Point out each Plasmodium parasite.
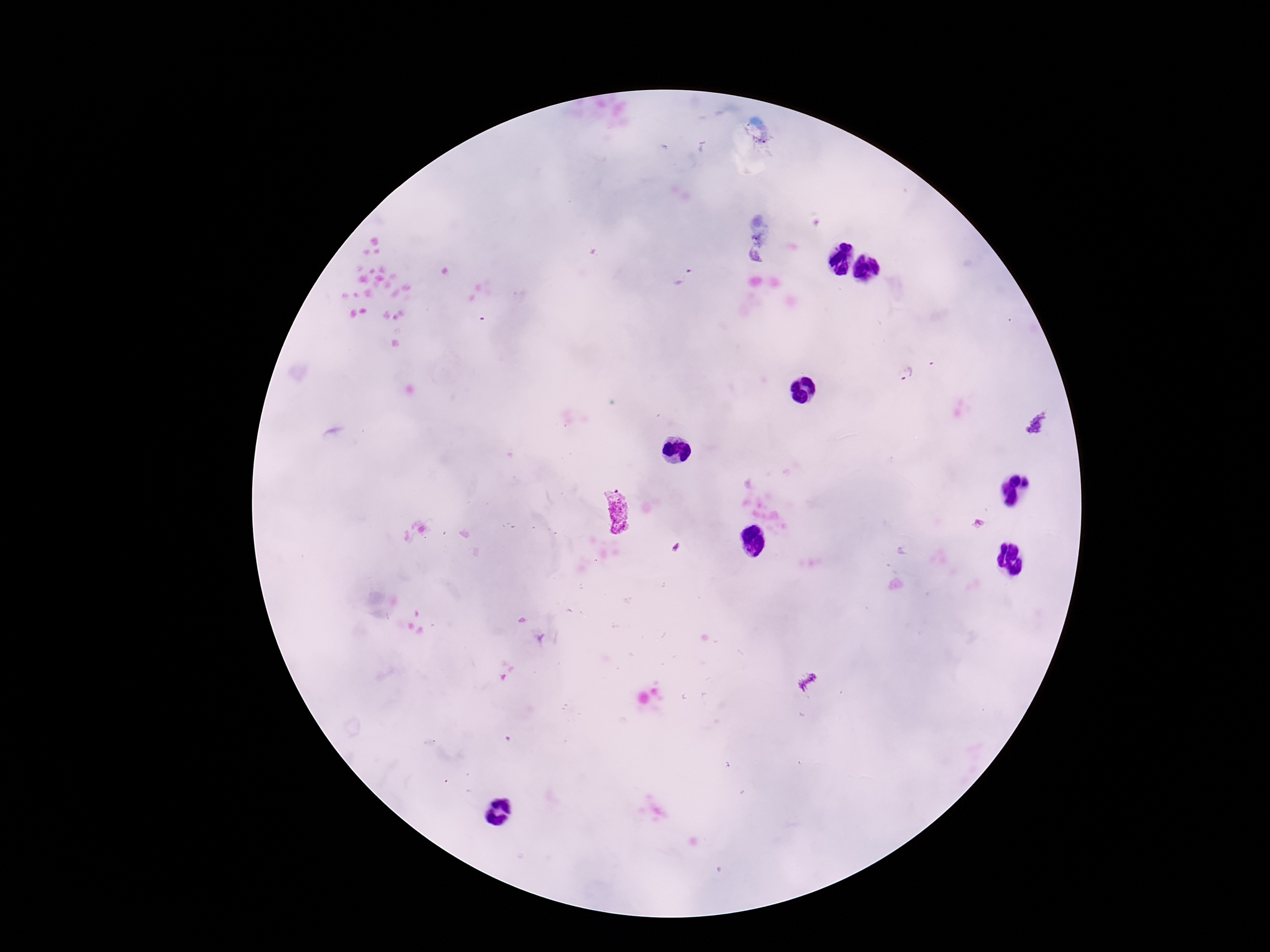

Approximate centers as (x, y) in pixels.
Plasmodium parasites: (755, 257), (683, 278), (904, 376), (616, 511), (978, 524).

100x magnification. Giemsa stain. Image is 1270×952 pixels. Single field of view. Smartphone photograph taken through the microscope eyepiece. Thick blood smear. Patient malaria status: positive.